Comment on the morphology of the erythrocytes.
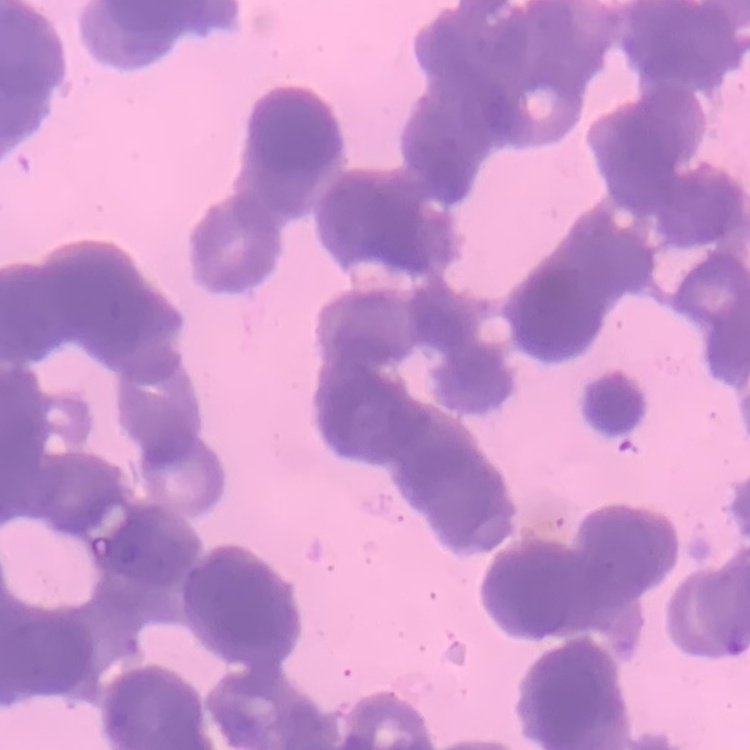

Rouleaux formation.

Stained with either Field's or Giemsa. Thin blood smear. One tile cut from a larger photomicrograph.